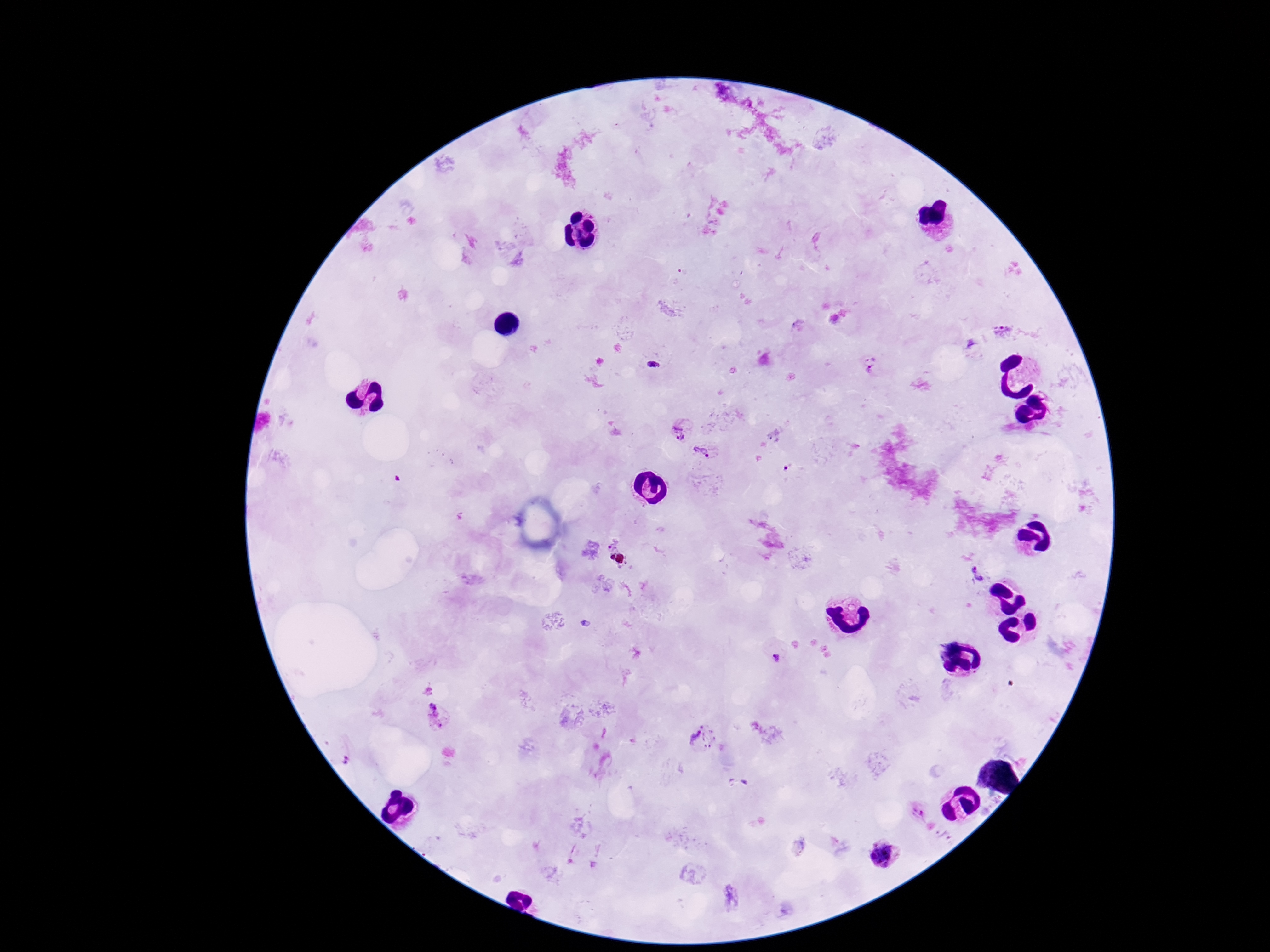
Approximate centers as [x, y] in pixels. Plasmodium parasite locations: [1005, 332], [653, 366], [871, 367], [680, 431], [703, 452], [789, 468], [982, 572], [775, 657], [436, 717], [701, 738], [346, 758], [919, 811], [884, 856]. One field from this slide. Image is 1270×952 pixels. Photographed through the microscope eyepiece with a smartphone camera. 100x magnification. Patient malaria status: infected. Giemsa stain. Thick blood smear.